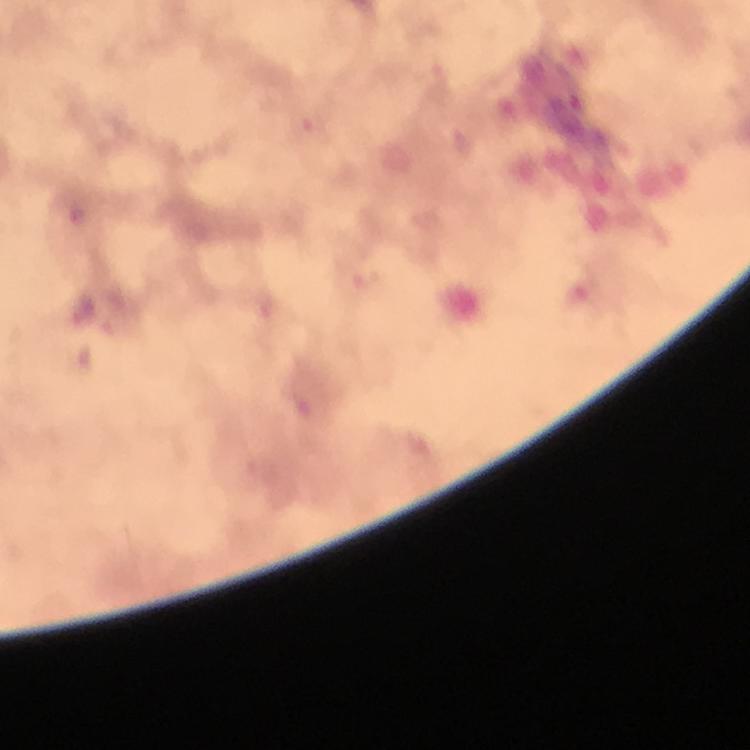
Approximate centers as {x, y} in pixels.
Summary:
  - Plasmodium parasite locations: {569, 101}
  - Cropped from: a single field of view
  - Capture: smartphone mounted on the microscope
  - Context: from a malaria diagnostic workup
  - Stain: Giemsa
  - Image size: 750×750 pixels
  - Immersion oil: used
  - Preparation: thick blood film
  - Magnification: 100x